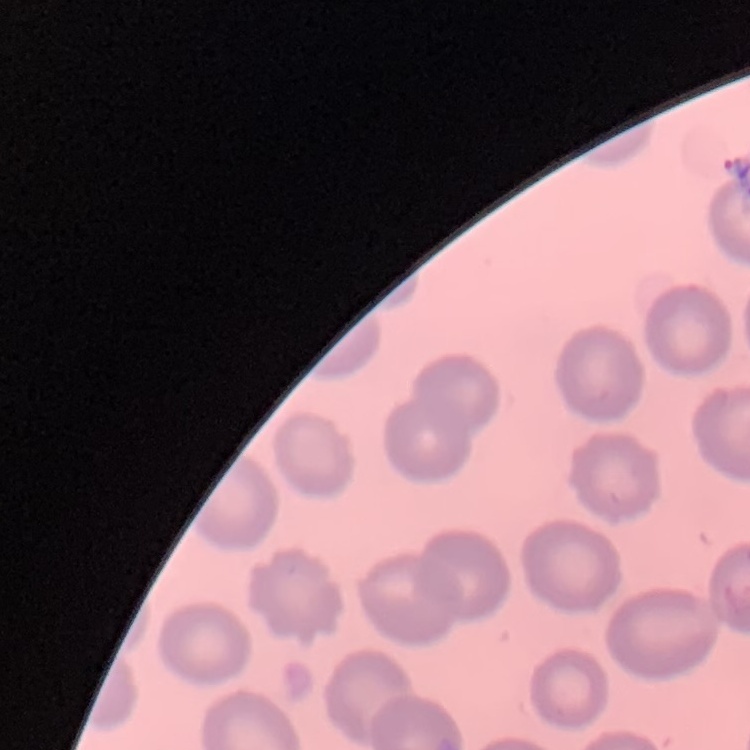 The red blood cells exhibit no rouleaux formation. Field's or Giemsa stain. One tile cut from a larger photomicrograph. Thin peripheral smear.